Point out each Plasmodium parasite.
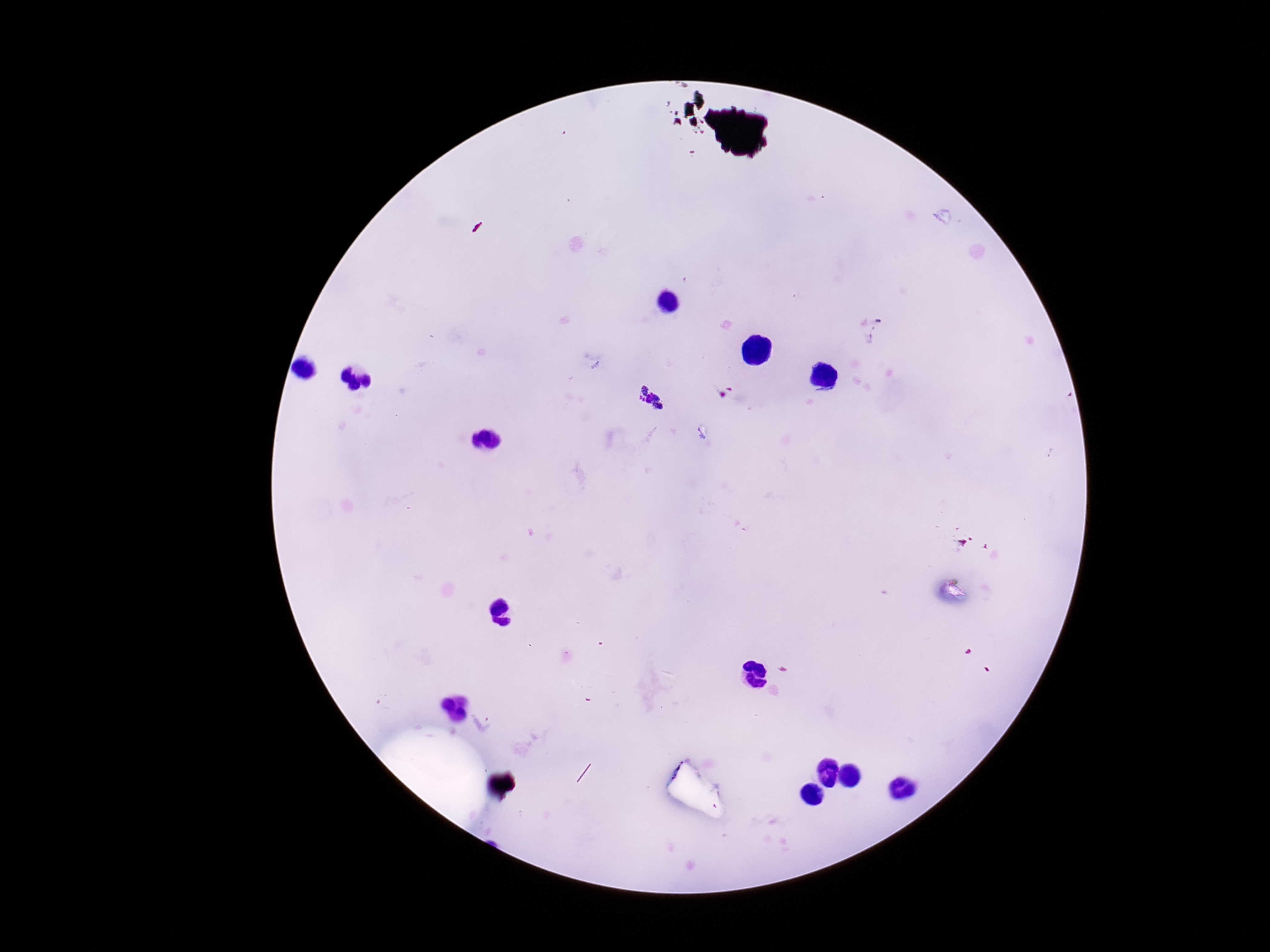

Approximate centers as {x, y} in pixels.
Plasmodium parasites: {649, 399}.

image size = 1270×952 pixels
capture = smartphone camera through the microscope eyepiece
magnification = 100x
preparation = thick blood smear
stain = Giemsa
field of view = single
patient malaria status = infected